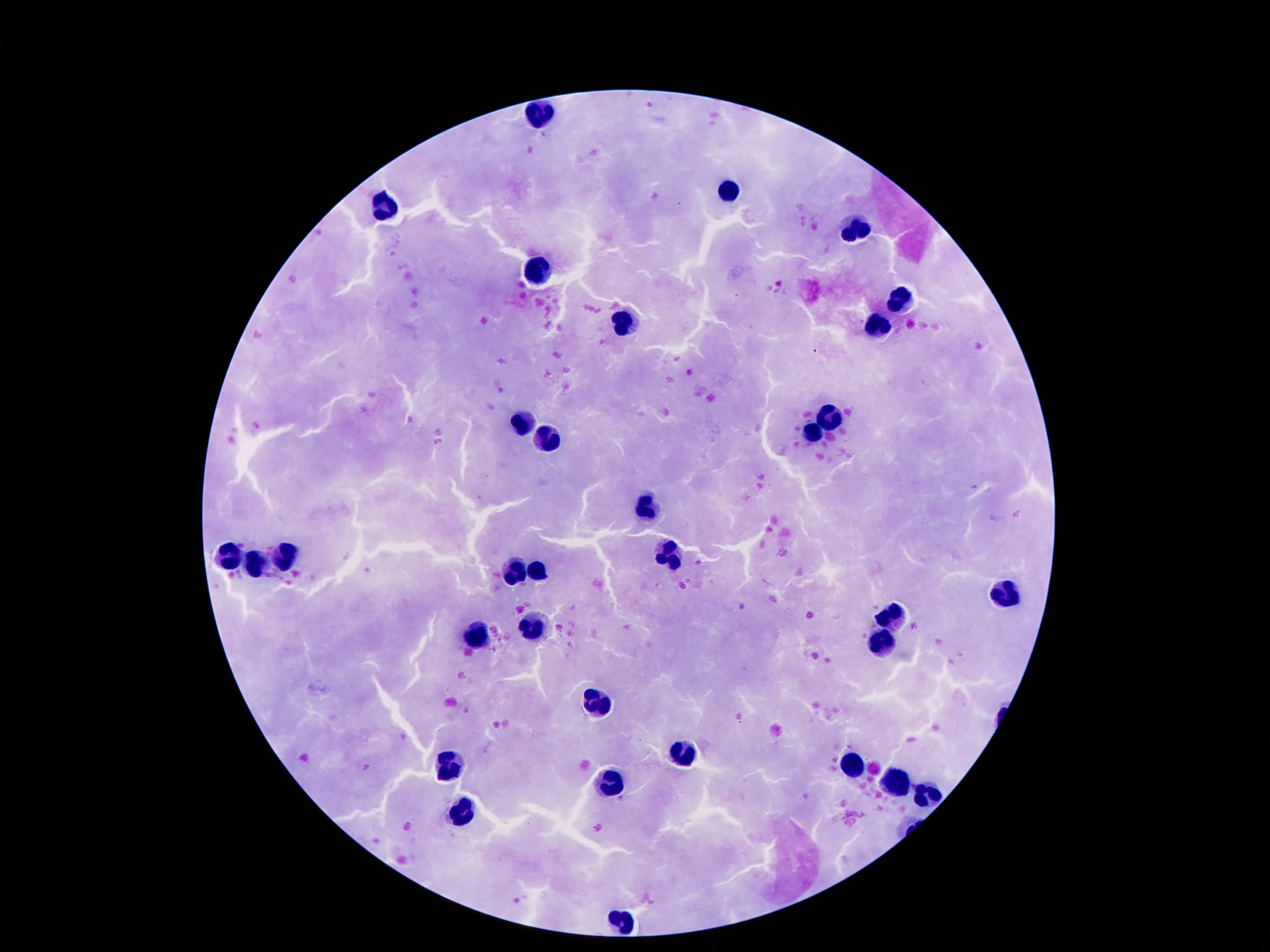

Approximate centers as [x, y] in pixels.
Summary:
  - Leukocyte locations: [539, 112], [732, 192], [383, 208], [853, 232], [539, 273], [898, 299], [623, 324], [879, 327], [827, 418], [523, 422], [812, 433], [547, 441], [644, 504], [287, 553], [668, 553], [228, 558], [254, 563], [517, 571], [539, 571], [1004, 593], [892, 616], [532, 624], [478, 633], [883, 639], [599, 700], [685, 756], [452, 764], [853, 764], [898, 782], [607, 784], [928, 797], [463, 814], [625, 921]
  - Stain: Giemsa
  - Field of view: one from this slide
  - Patient malaria status: negative
  - Capture: smartphone camera through the microscope eyepiece
  - Preparation: thick peripheral-blood smear
  - Magnification: 100x
  - Image size: 1270×952 pixels